Identify the parasite.
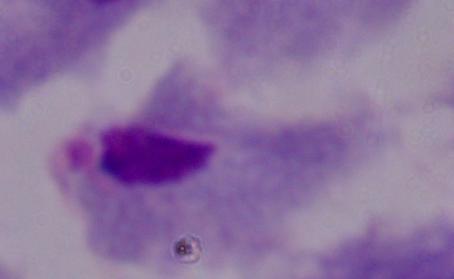
This is a trichomonad.

Micrograph. 1000x magnification.